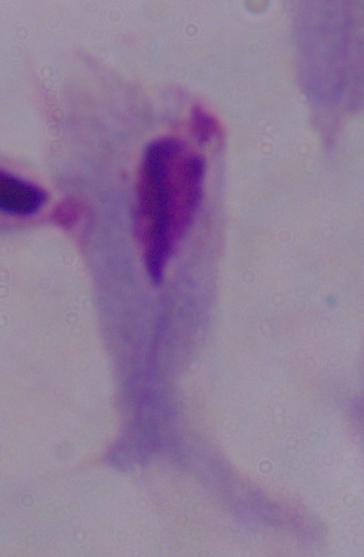
{
  "identification": "trichomonad",
  "magnification": "1000x",
  "modality": "micrograph"
}